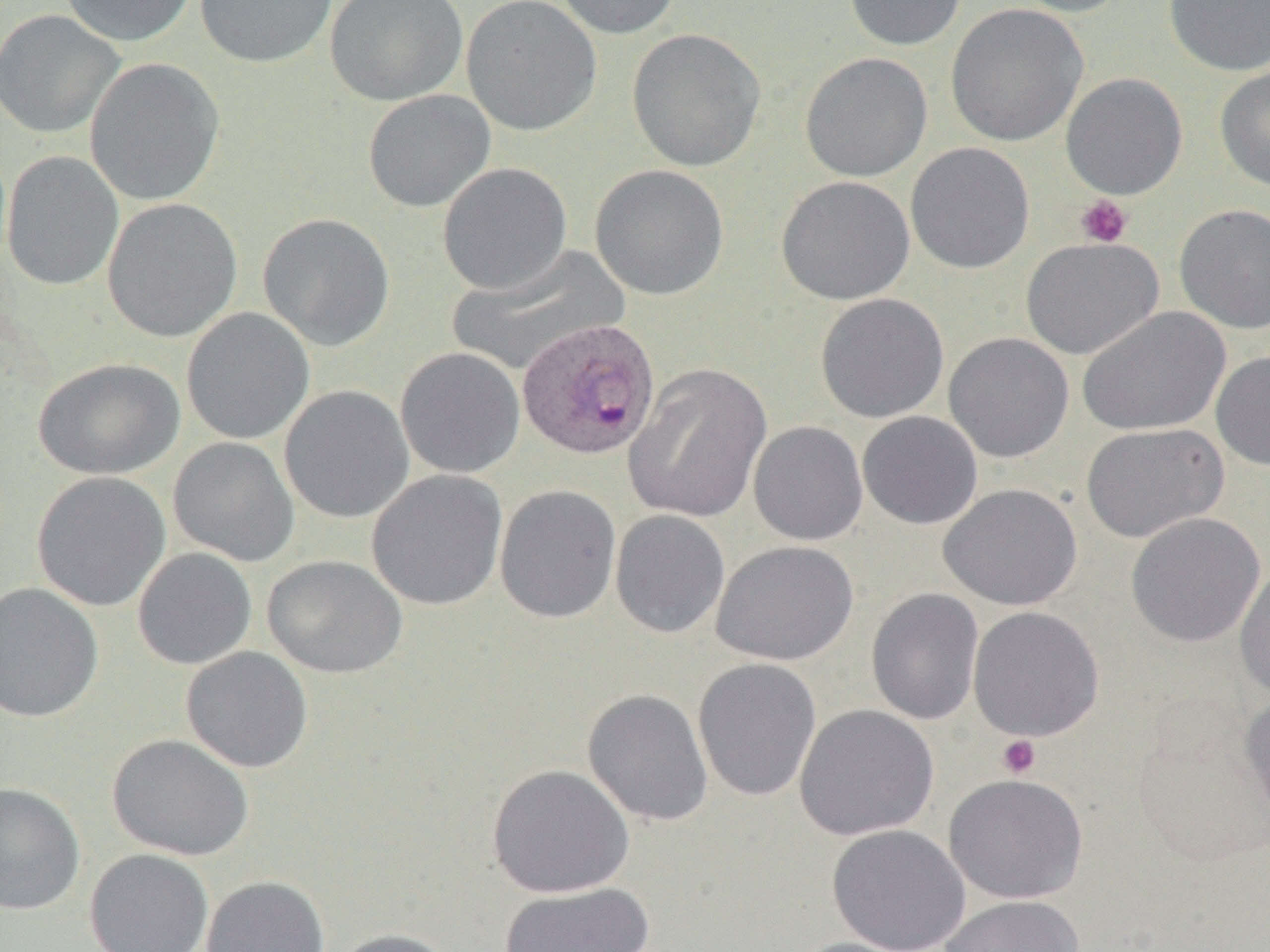
Approximate bounding boxes as (x1, y1, x2, y2) in pixels. Uninfected red blood cell locations: (59, 0, 196, 47), (195, 0, 338, 69), (324, 0, 468, 106), (461, 0, 603, 136), (553, 0, 685, 39), (844, 0, 967, 51), (1009, 0, 1134, 18), (1164, 0, 1270, 76), (945, 3, 1088, 147), (0, 9, 125, 139), (626, 28, 766, 172), (799, 52, 932, 182), (85, 58, 225, 206), (1214, 63, 1270, 192), (1060, 73, 1188, 199), (362, 89, 496, 213), (905, 142, 1035, 274), (1, 150, 124, 291), (437, 162, 573, 295), (590, 164, 729, 300), (776, 175, 915, 305), (102, 197, 243, 343), (1173, 203, 1270, 334), (257, 212, 396, 351), (1020, 236, 1164, 360), (446, 244, 629, 376), (815, 293, 949, 423), (1077, 306, 1231, 436), (181, 307, 315, 444), (943, 332, 1074, 463), (395, 347, 526, 479), (1210, 350, 1270, 471), (33, 357, 185, 480), (624, 363, 772, 523), (279, 385, 414, 523), (857, 411, 983, 530), (748, 420, 868, 546), (1080, 422, 1228, 542), (168, 437, 300, 567), (366, 469, 508, 611), (31, 471, 171, 612), (938, 483, 1082, 610), (494, 484, 622, 623), (610, 510, 730, 639), (1125, 512, 1265, 648), (710, 540, 858, 665), (132, 547, 257, 670), (262, 555, 408, 679), (1234, 561, 1270, 702), (0, 582, 103, 723), (866, 588, 984, 725), (968, 606, 1105, 741), (181, 646, 313, 773), (692, 657, 822, 802), (582, 688, 714, 826), (1238, 689, 1270, 832), (794, 704, 939, 841), (1131, 712, 1270, 868), (107, 733, 254, 861), (486, 764, 635, 898), (944, 773, 1087, 903), (0, 782, 85, 915), (826, 824, 970, 952), (84, 848, 214, 952), (200, 875, 330, 952), (497, 881, 655, 952), (938, 895, 1084, 952), (327, 928, 458, 952), (788, 937, 920, 952). Platelet locations: (1075, 194, 1133, 248), (996, 735, 1041, 779). Plasmodium ovale-infected red blood cell locations: (514, 319, 658, 462). Slide-level diagnosis: Plasmodium ovale. Image is 1270×952 pixels. Light microscopy. One field of a larger specimen. 1000x magnification. Thin blood smear.